Comment on the morphology of the erythrocytes.
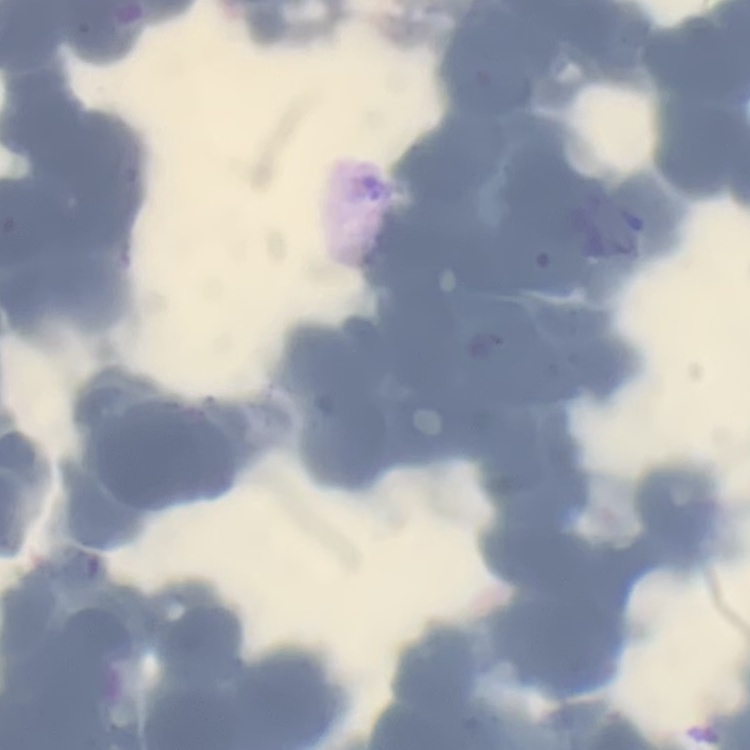
Rouleaux formation.

image type = square crop of a larger photomicrograph
preparation = thin blood film
stain = Field's or Giemsa